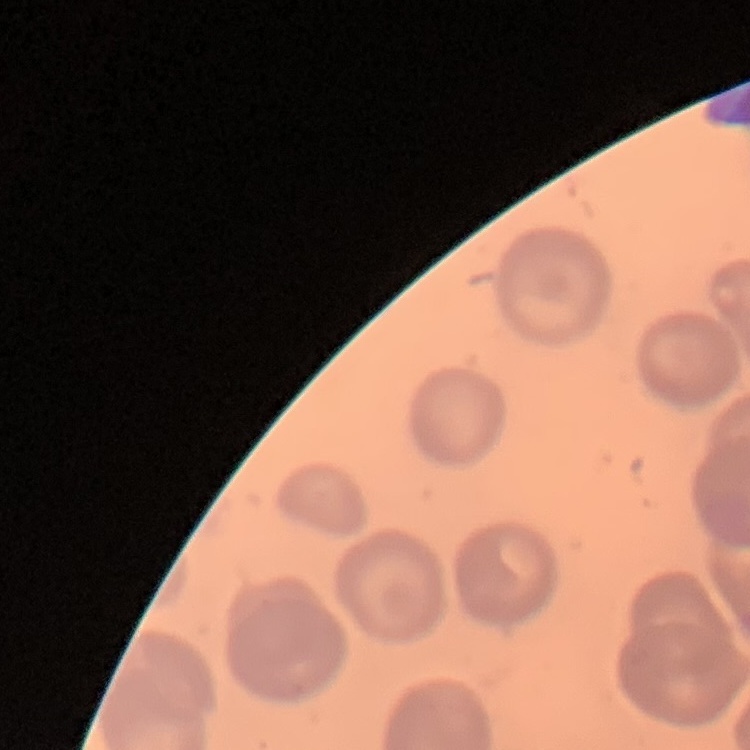 The red blood cells show no rouleaux formation. Field's or Giemsa stain. One tile cut from a larger photomicrograph. Thin blood smear.